Evaluate for malaria.
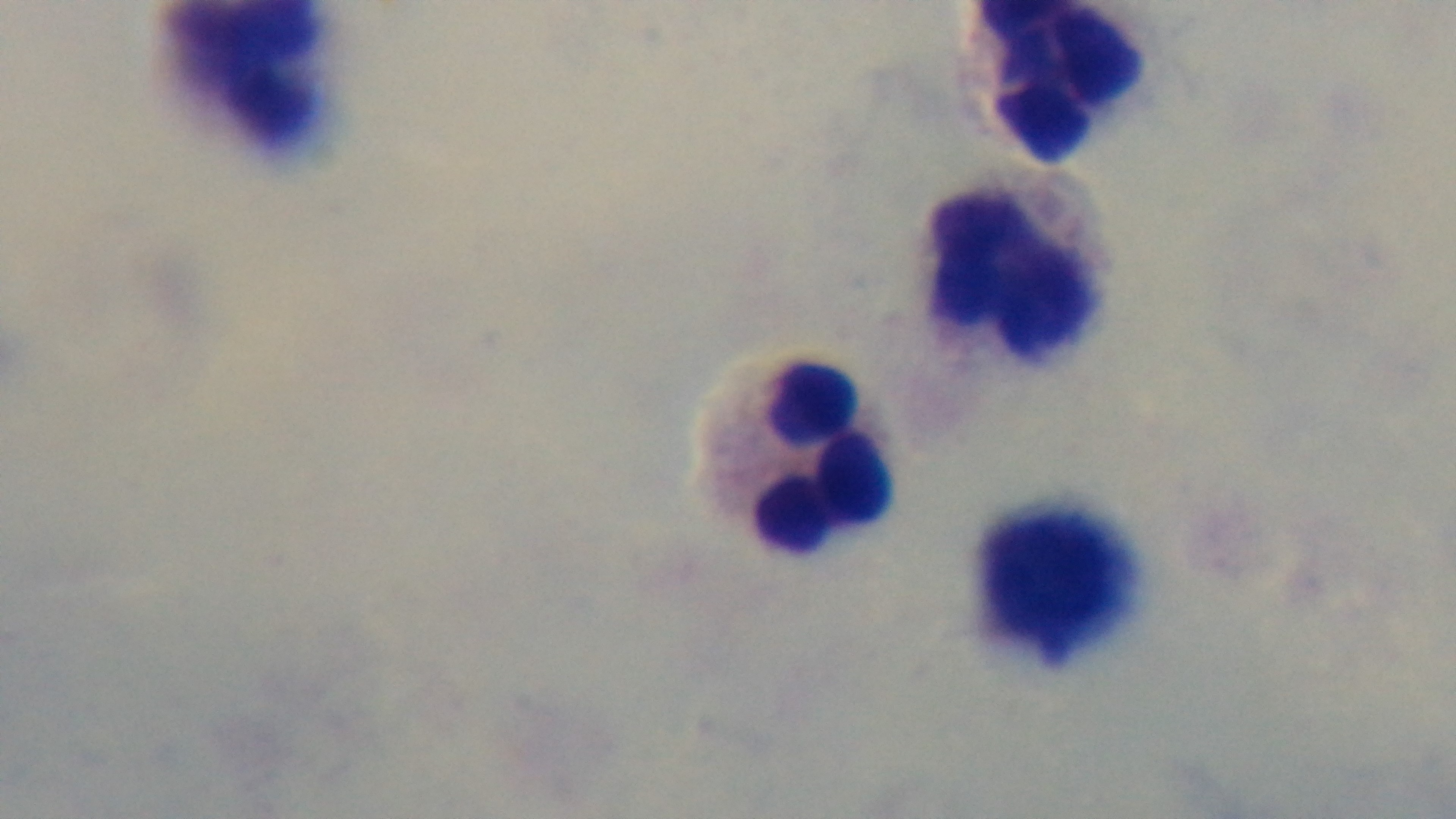

It is uninfected.

Summary:
  - Preparation: thick blood film
  - Field of view: single
  - Objective: 100x oil immersion
  - Stain: Giemsa
  - Capture: mounted 4K digital camera
  - Modality: light microscopy